State which parasite is depicted.
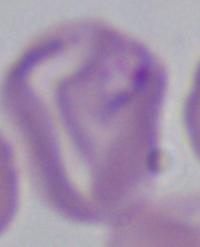

Babesia.

modality = photomicrograph
magnification = 1000x